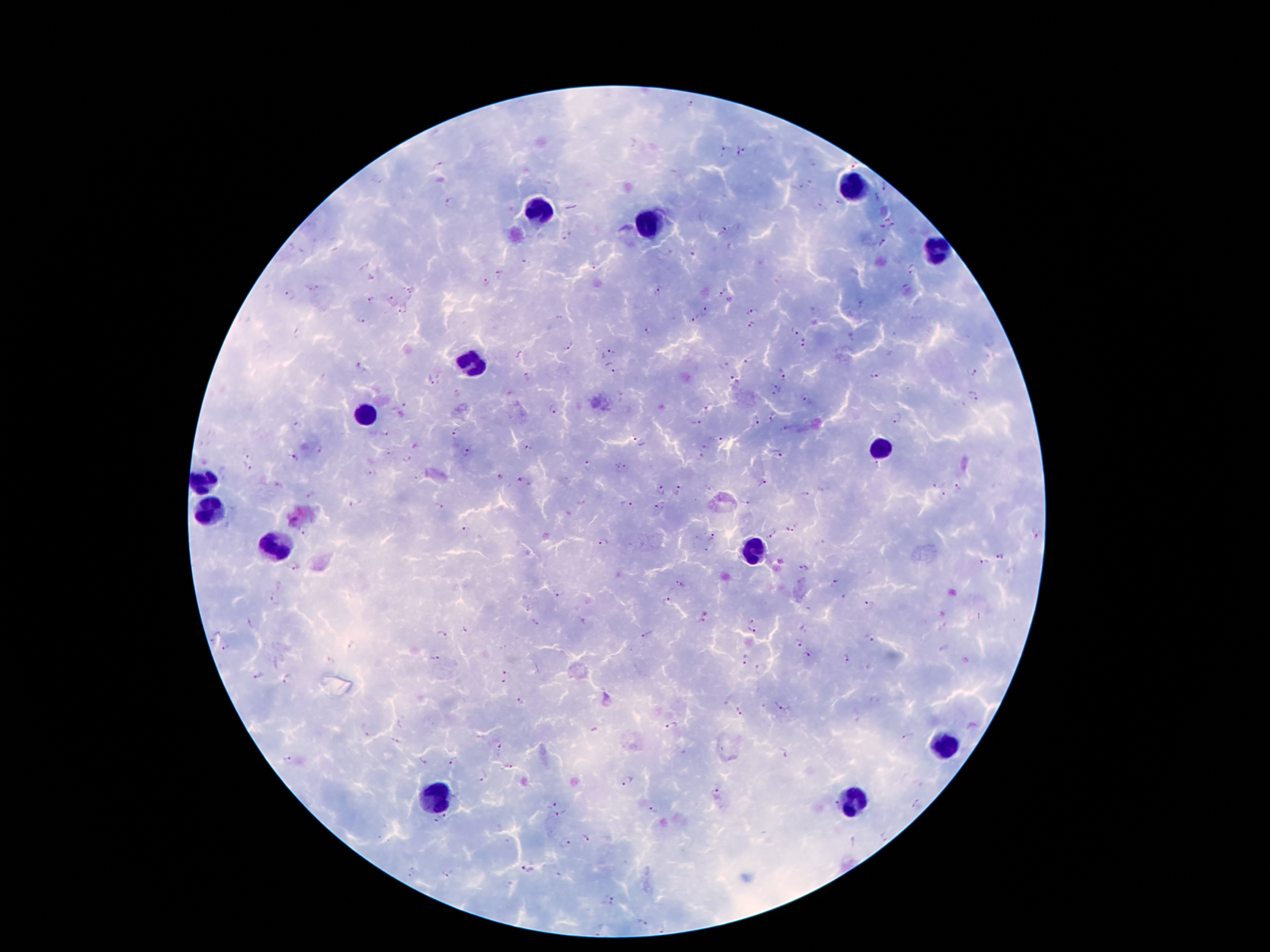
coordinate format = approximate object centers, in pixels from the top-left corner
Plasmodium parasite locations = (x=691, y=103), (x=723, y=149), (x=743, y=151), (x=440, y=166), (x=856, y=167), (x=887, y=185), (x=876, y=197), (x=448, y=200), (x=838, y=203), (x=726, y=231), (x=569, y=236), (x=883, y=243), (x=694, y=254), (x=524, y=262), (x=595, y=267), (x=911, y=269), (x=500, y=273), (x=485, y=282), (x=410, y=290), (x=658, y=291), (x=720, y=292), (x=290, y=295), (x=371, y=300), (x=391, y=300), (x=404, y=311), (x=753, y=311), (x=705, y=313), (x=693, y=319), (x=361, y=320), (x=753, y=327), (x=647, y=331), (x=794, y=333), (x=804, y=343), (x=570, y=345), (x=603, y=351), (x=748, y=360), (x=361, y=366), (x=610, y=368), (x=972, y=371), (x=783, y=373), (x=873, y=376), (x=528, y=377), (x=431, y=380), (x=733, y=381), (x=777, y=386), (x=974, y=396), (x=804, y=398), (x=404, y=407), (x=555, y=407), (x=706, y=411), (x=773, y=417), (x=898, y=418), (x=756, y=421), (x=297, y=424), (x=695, y=424), (x=456, y=431), (x=384, y=435), (x=721, y=439), (x=640, y=440), (x=705, y=446), (x=528, y=447), (x=320, y=450), (x=468, y=452), (x=778, y=455), (x=700, y=457), (x=296, y=458), (x=406, y=459), (x=588, y=463), (x=629, y=466), (x=876, y=466), (x=247, y=467), (x=618, y=469), (x=373, y=473), (x=499, y=477), (x=519, y=480), (x=764, y=484), (x=934, y=485), (x=959, y=487), (x=662, y=489), (x=679, y=489), (x=806, y=495), (x=944, y=496), (x=745, y=503), (x=438, y=506), (x=625, y=506), (x=659, y=507), (x=790, y=529), (x=465, y=531), (x=304, y=534), (x=771, y=535), (x=713, y=536), (x=605, y=542), (x=998, y=556), (x=983, y=561), (x=293, y=567), (x=804, y=568), (x=680, y=582), (x=835, y=582), (x=558, y=593), (x=274, y=598), (x=667, y=601), (x=870, y=604), (x=751, y=619), (x=583, y=621), (x=534, y=623), (x=751, y=630), (x=440, y=633), (x=647, y=634), (x=870, y=637), (x=798, y=644), (x=227, y=647), (x=807, y=655), (x=435, y=657), (x=846, y=658), (x=744, y=661), (x=760, y=670), (x=505, y=673), (x=260, y=675), (x=287, y=678), (x=503, y=681), (x=521, y=699), (x=781, y=706), (x=740, y=711), (x=672, y=725), (x=909, y=736), (x=395, y=740), (x=499, y=746), (x=782, y=753), (x=285, y=761), (x=424, y=761), (x=453, y=761), (x=510, y=766), (x=483, y=777), (x=628, y=781), (x=715, y=792), (x=833, y=802), (x=916, y=803), (x=552, y=804), (x=652, y=808), (x=445, y=815), (x=561, y=815), (x=436, y=822), (x=585, y=836), (x=884, y=837), (x=566, y=843), (x=529, y=871), (x=413, y=872), (x=448, y=874), (x=610, y=901), (x=642, y=923), (x=663, y=928)
leukocyte locations = (x=851, y=184), (x=535, y=214), (x=646, y=224), (x=936, y=253), (x=470, y=359), (x=365, y=417), (x=877, y=447), (x=201, y=482), (x=213, y=512), (x=274, y=545), (x=757, y=550), (x=944, y=743), (x=434, y=797), (x=856, y=799)
preparation = thick peripheral-blood smear
patient malaria status = infected with Plasmodium falciparum
stain = Giemsa
capture = smartphone through the microscope eyepiece
field of view = single
image size = 1270×952 pixels
magnification = 100x